Locate platelets.
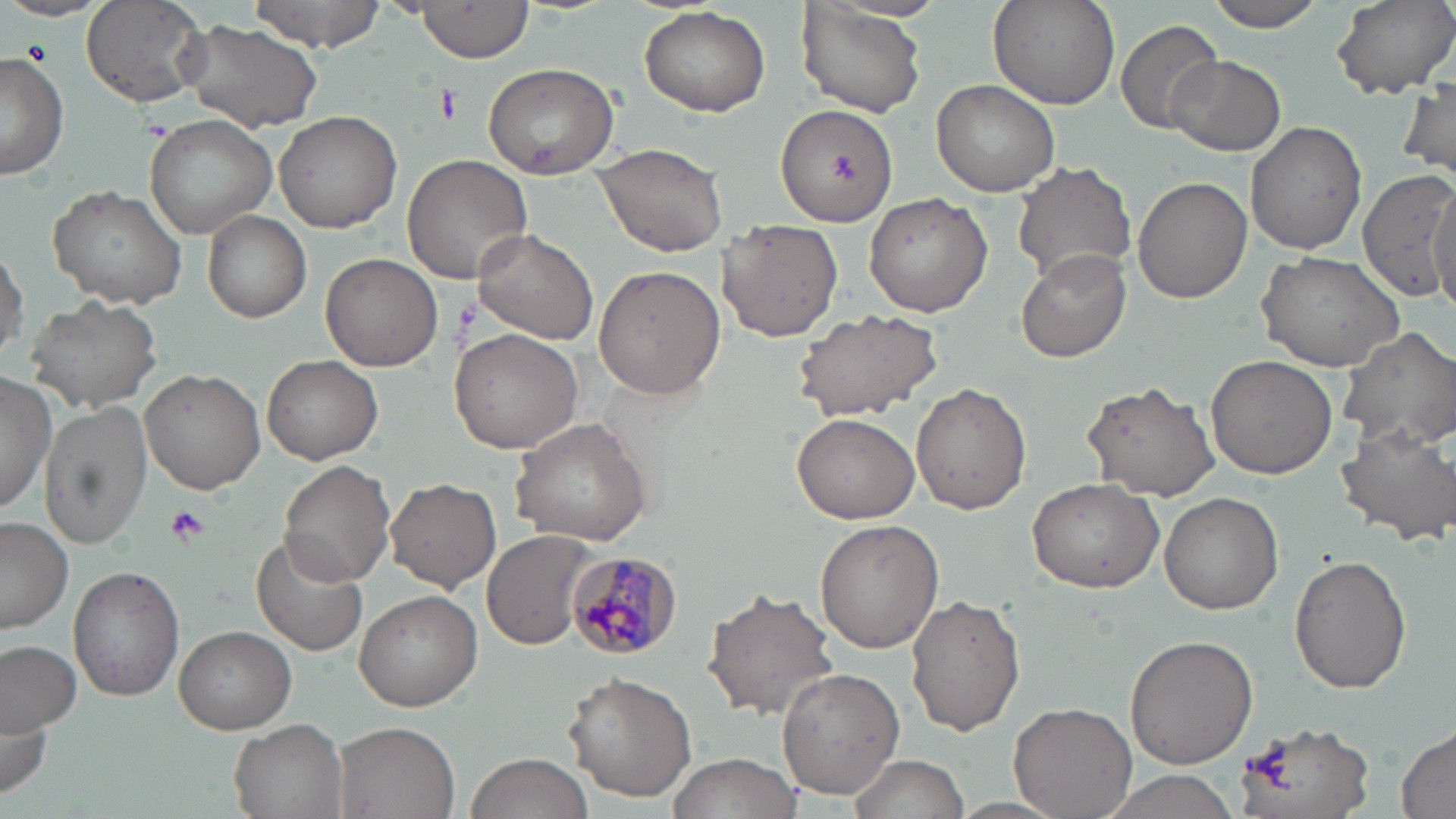

Approximate bounding boxes as named x1/y1/x2/y2 corners in pixels.
Platelets: (x1=433, y1=86, x2=462, y2=127), (x1=164, y1=505, x2=210, y2=547).

Uninfected red blood cell locations: (x1=246, y1=0, x2=389, y2=51), (x1=989, y1=0, x2=1119, y2=110), (x1=1202, y1=0, x2=1330, y2=31), (x1=1330, y1=0, x2=1456, y2=101), (x1=0, y1=1, x2=110, y2=23), (x1=81, y1=1, x2=211, y2=110), (x1=414, y1=1, x2=535, y2=62), (x1=798, y1=2, x2=929, y2=118), (x1=639, y1=6, x2=770, y2=117), (x1=179, y1=15, x2=327, y2=135), (x1=1117, y1=19, x2=1224, y2=135), (x1=0, y1=52, x2=71, y2=181), (x1=1165, y1=55, x2=1285, y2=158), (x1=482, y1=62, x2=621, y2=180), (x1=1399, y1=76, x2=1456, y2=185), (x1=930, y1=80, x2=1061, y2=198), (x1=775, y1=102, x2=898, y2=228), (x1=274, y1=108, x2=403, y2=233), (x1=144, y1=114, x2=278, y2=241), (x1=1245, y1=121, x2=1367, y2=255), (x1=592, y1=142, x2=729, y2=258), (x1=400, y1=153, x2=532, y2=285), (x1=1011, y1=161, x2=1137, y2=287), (x1=1354, y1=170, x2=1455, y2=302), (x1=1133, y1=175, x2=1251, y2=305), (x1=1428, y1=181, x2=1456, y2=307), (x1=47, y1=185, x2=189, y2=310), (x1=864, y1=191, x2=993, y2=318), (x1=202, y1=210, x2=312, y2=324), (x1=717, y1=217, x2=844, y2=342), (x1=474, y1=229, x2=600, y2=347), (x1=0, y1=245, x2=26, y2=364), (x1=1015, y1=247, x2=1133, y2=363), (x1=1254, y1=250, x2=1406, y2=371), (x1=321, y1=251, x2=443, y2=371), (x1=594, y1=266, x2=725, y2=399), (x1=26, y1=294, x2=162, y2=414), (x1=790, y1=306, x2=943, y2=421), (x1=1337, y1=326, x2=1456, y2=453), (x1=452, y1=328, x2=584, y2=455), (x1=1206, y1=353, x2=1339, y2=479), (x1=261, y1=354, x2=383, y2=464), (x1=139, y1=367, x2=266, y2=495), (x1=0, y1=372, x2=56, y2=516), (x1=1081, y1=380, x2=1220, y2=501), (x1=912, y1=382, x2=1031, y2=514), (x1=39, y1=400, x2=152, y2=548), (x1=792, y1=412, x2=919, y2=524), (x1=509, y1=416, x2=651, y2=545), (x1=1334, y1=422, x2=1456, y2=543), (x1=278, y1=461, x2=396, y2=587), (x1=1026, y1=476, x2=1165, y2=593), (x1=385, y1=477, x2=501, y2=593), (x1=1160, y1=492, x2=1283, y2=613), (x1=0, y1=517, x2=73, y2=633), (x1=815, y1=520, x2=943, y2=653), (x1=482, y1=530, x2=594, y2=651), (x1=250, y1=531, x2=370, y2=657), (x1=1289, y1=554, x2=1412, y2=694), (x1=67, y1=564, x2=182, y2=701), (x1=704, y1=584, x2=842, y2=722), (x1=354, y1=590, x2=482, y2=711), (x1=907, y1=594, x2=1025, y2=737), (x1=174, y1=624, x2=296, y2=733), (x1=1124, y1=634, x2=1258, y2=768), (x1=0, y1=639, x2=81, y2=735), (x1=776, y1=669, x2=905, y2=798), (x1=562, y1=672, x2=697, y2=802), (x1=1, y1=689, x2=53, y2=806), (x1=1010, y1=699, x2=1138, y2=819), (x1=228, y1=719, x2=348, y2=819), (x1=334, y1=721, x2=461, y2=818), (x1=1233, y1=722, x2=1373, y2=819), (x1=1393, y1=723, x2=1456, y2=819), (x1=466, y1=751, x2=595, y2=819), (x1=667, y1=751, x2=804, y2=819), (x1=844, y1=753, x2=969, y2=819), (x1=1099, y1=771, x2=1246, y2=818), (x1=949, y1=796, x2=1070, y2=817). Plasmodium malariae-infected red blood cell locations: (x1=565, y1=549, x2=681, y2=663). Slide-level diagnosis: Plasmodium malariae. 1000x magnification. Image is 1456×819 pixels. Single field of view. Optical microscopy. May-Grünwald-Giemsa-stained preparation. Thin blood film.